State which parasite is depicted.
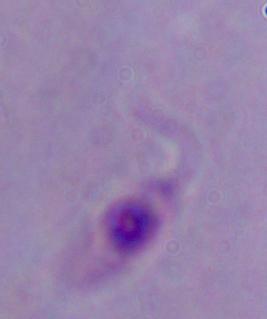
Leishmania.

Captured at 1000x magnification. Micrograph.